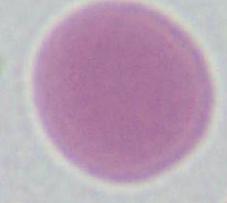

Micrograph. An erythrocyte is shown. 1000x magnification.